Evaluate for malaria.
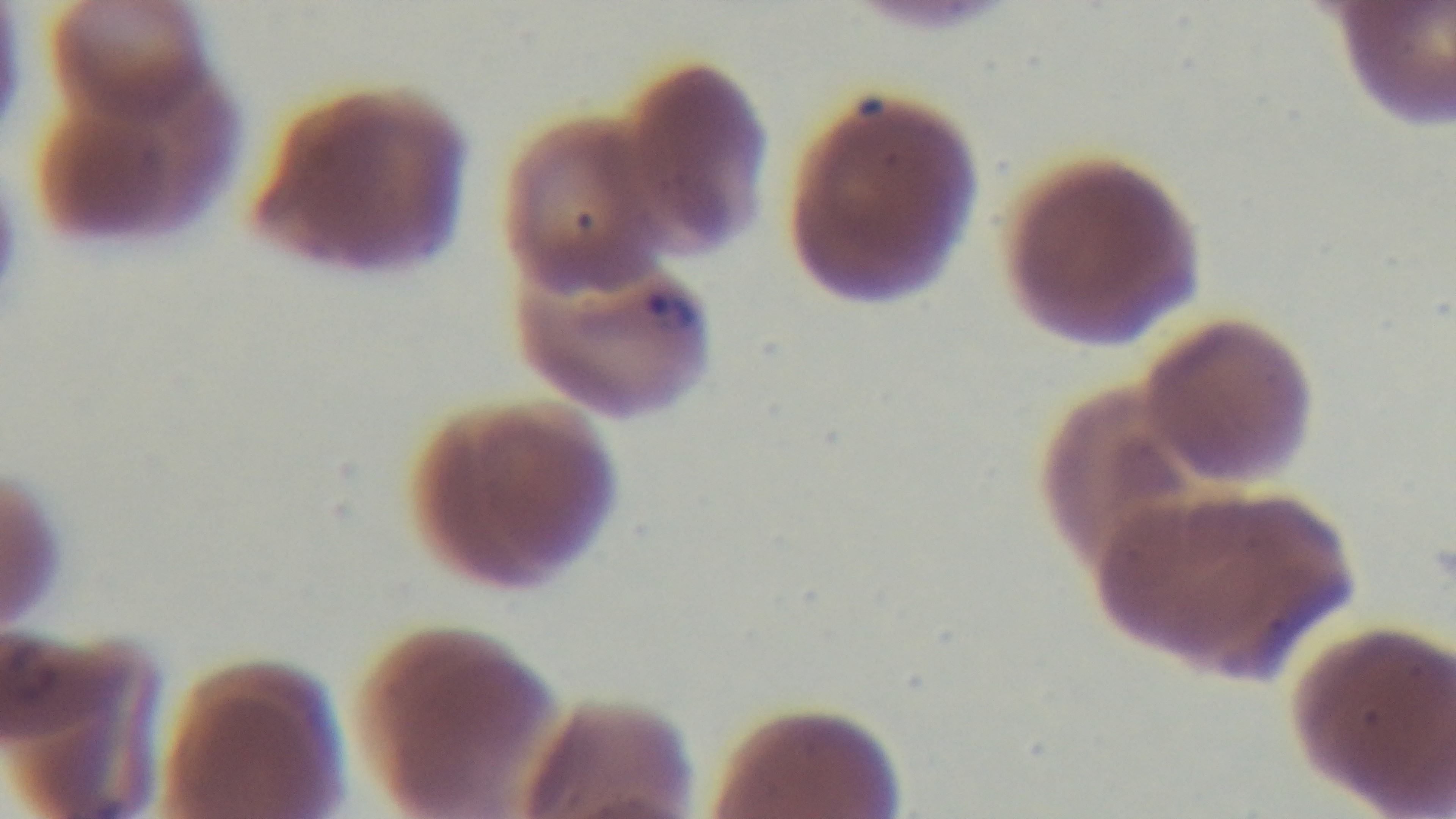
Infected.

capture = mounted 4K digital camera
field of view = single
modality = light microscopy
stain = Giemsa
objective = 100x oil immersion
preparation = thin blood film